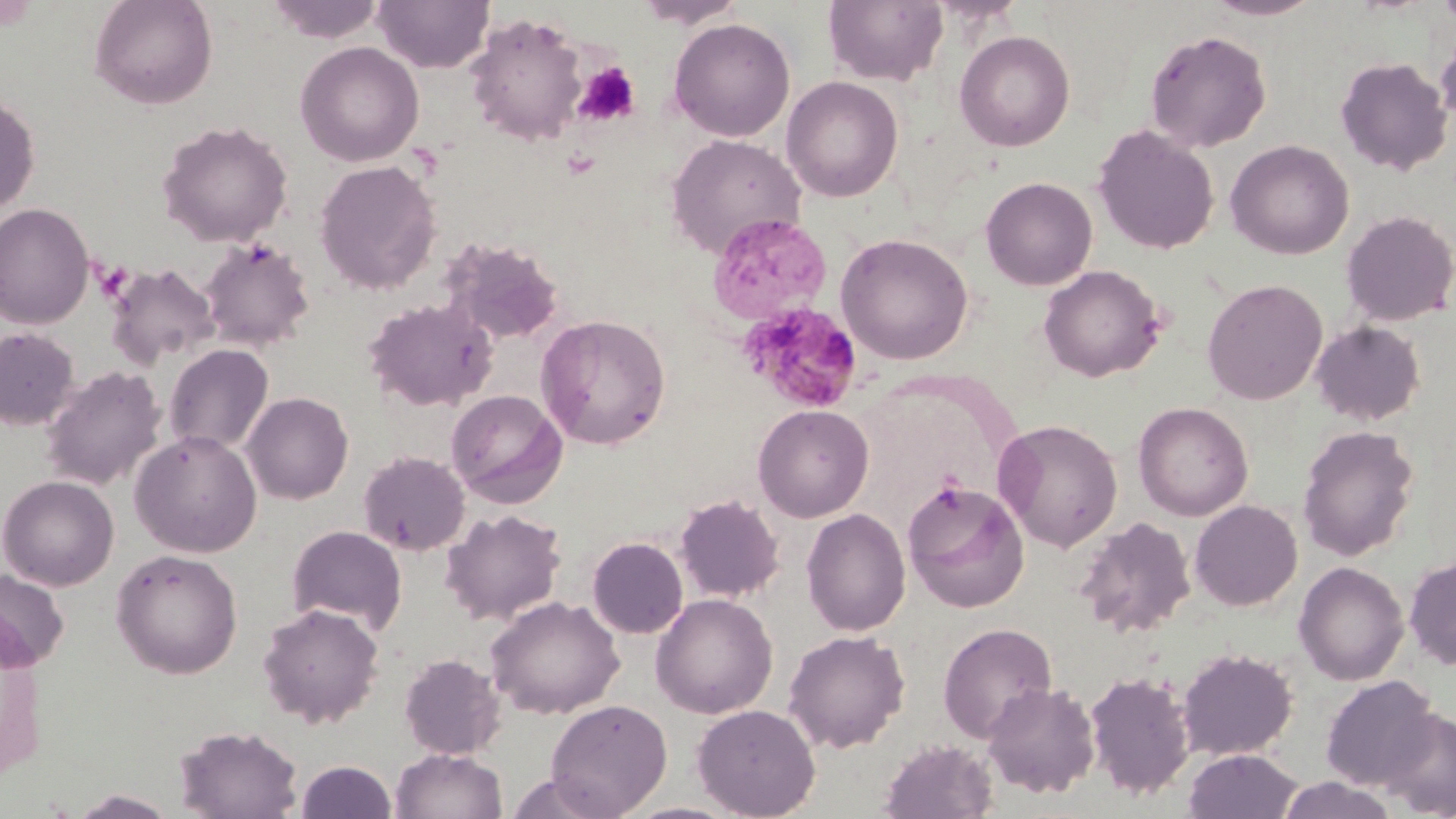
{
  "plasmodium_malariae_infected_red_blood_cell_locations": "approximate bounding boxes as (x1,y1)-(x2,y2) corner pairs in pixels: (740,300)-(864,412)",
  "slide_level_diagnosis": "Plasmodium malariae",
  "magnification": "1000x",
  "preparation": "thin blood film",
  "uninfected_red_blood_cell_locations": "approximate bounding boxes as (x1,y1)-(x2,y2) corner pairs in pixels: (88,0)-(219,109), (265,0)-(386,43), (373,0)-(494,73), (632,0)-(747,28), (824,0)-(949,86), (1202,0)-(1325,21), (1435,0)-(1456,31), (464,13)-(589,148), (668,18)-(796,142), (1435,24)-(1456,128), (954,30)-(1075,151), (1144,30)-(1272,152), (295,41)-(424,167), (1335,57)-(1453,176), (781,76)-(904,202), (0,94)-(40,216), (157,120)-(293,247), (1094,125)-(1219,255), (665,133)-(806,259), (1226,140)-(1354,260), (314,159)-(443,295), (980,176)-(1098,290), (0,203)-(94,329), (1341,210)-(1456,326), (707,213)-(832,325), (836,232)-(973,364), (199,236)-(316,352), (441,236)-(565,347), (107,263)-(220,371), (1039,264)-(1166,382), (1202,278)-(1328,404), (364,298)-(497,412), (535,313)-(671,449), (1311,320)-(1427,426), (0,327)-(79,430), (164,344)-(274,456), (42,366)-(166,491), (446,389)-(568,508), (242,392)-(353,504), (1133,402)-(1253,521), (753,404)-(874,522), (993,418)-(1124,552), (1297,424)-(1419,561), (129,430)-(263,557), (358,450)-(470,555), (1,474)-(119,590), (901,478)-(1029,612), (674,494)-(786,603), (1190,500)-(1302,610), (440,508)-(567,625), (801,508)-(912,637), (1074,516)-(1196,638), (287,525)-(407,635), (587,537)-(688,639), (111,548)-(244,679), (1404,554)-(1456,670), (1293,561)-(1409,685), (0,569)-(70,672), (650,593)-(778,718), (485,596)-(624,718), (257,603)-(384,728), (938,622)-(1057,742), (783,629)-(910,752), (1177,648)-(1298,760), (399,653)-(507,760), (1084,670)-(1195,800), (1319,674)-(1440,791), (982,682)-(1101,799), (545,698)-(673,817), (692,703)-(821,818), (1378,707)-(1456,818), (175,723)-(304,818), (879,738)-(998,819), (389,747)-(508,819), (1183,749)-(1304,819), (295,760)-(398,819), (504,771)-(618,818), (1275,776)-(1401,819), (67,788)-(180,818)",
  "platelet_locations": "approximate bounding boxes as (x1,y1)-(x2,y2) corner pairs in pixels: (574,63)-(640,127)",
  "field_of_view": "one of a larger specimen",
  "stain": "May-Grünwald-Giemsa",
  "modality": "optical microscopy",
  "image_size": "1456×819 pixels"
}